Comment on the morphology of the red blood cells.
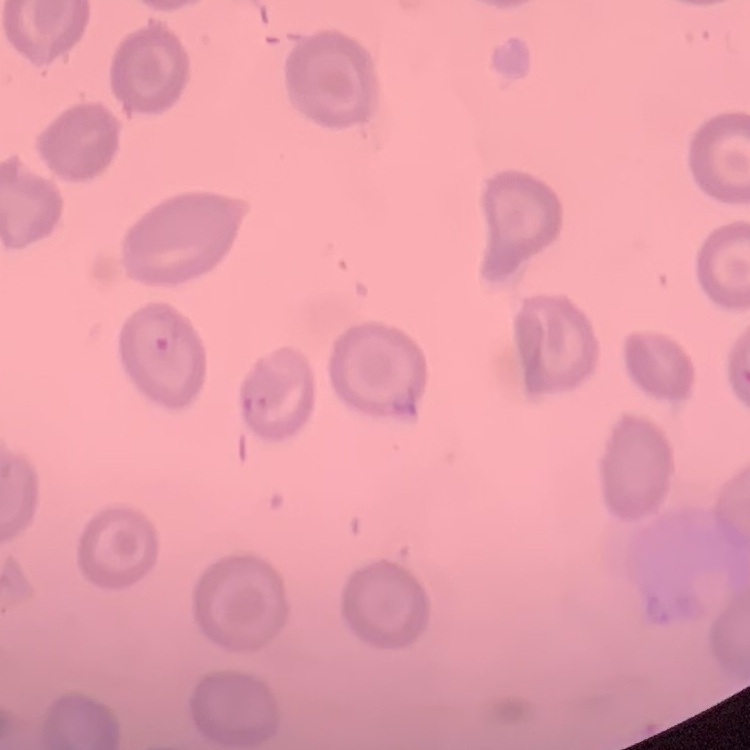

No rouleaux formation.

preparation: thin blood smear
stain: Field's or Giemsa
image_type: square crop of a larger photomicrograph